Assess this cell for malaria.
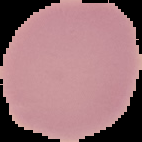
It is uninfected.

The area outside the segmented cell region is set to black. From a thin blood smear. Image is 142×142 pixels.